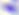

identification = Toxoplasma gondii
modality = micrograph
magnification = 400x